Give the extent of all Plasmodium falciparum-infected red blood cells.
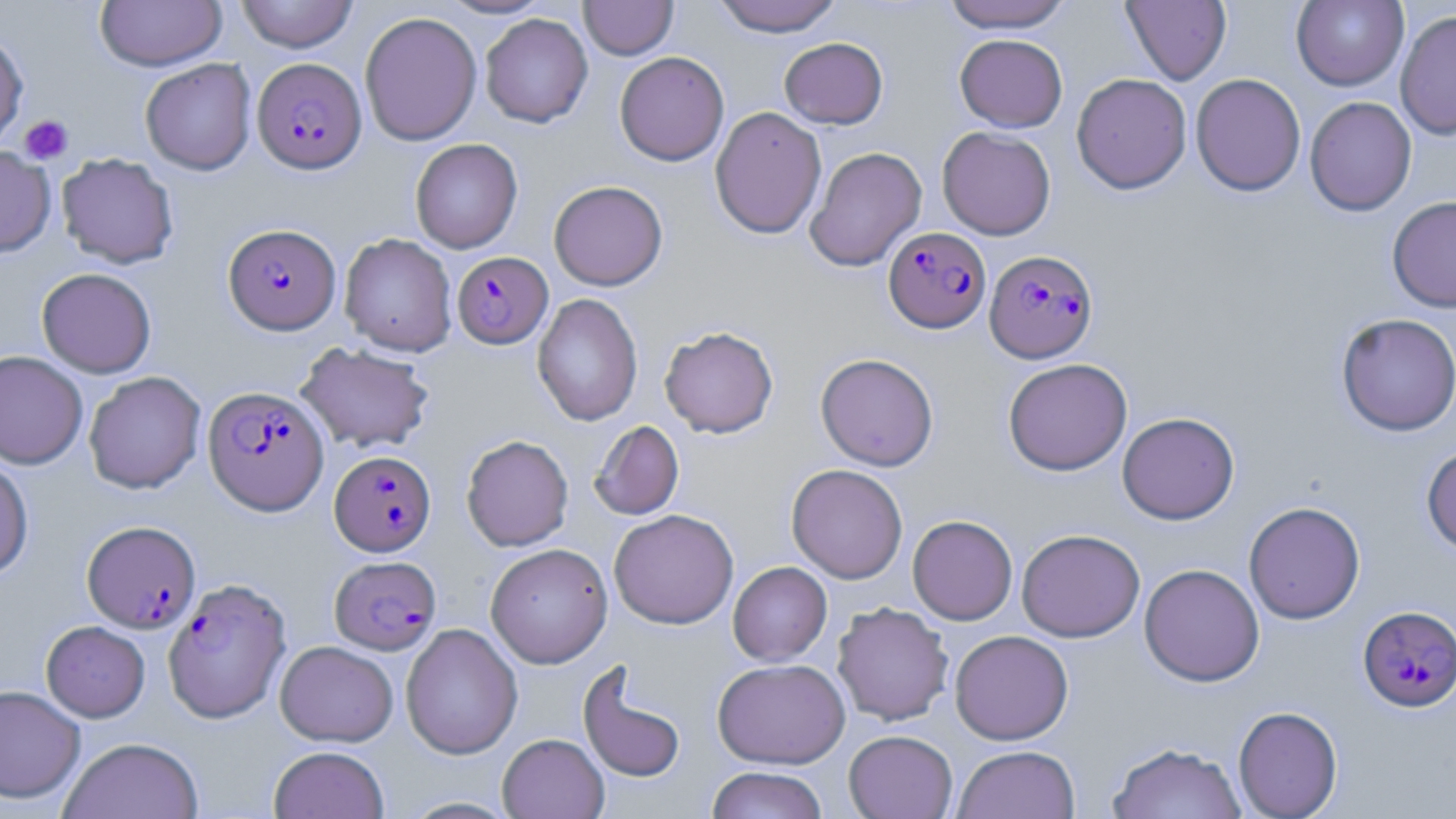

Approximate bounding boxes as (x1,y1)-(x2,y2) corner pairs in pixels.
Plasmodium falciparum-infected red blood cells: (252,57)-(366,173), (223,223)-(340,334), (883,227)-(991,333), (984,249)-(1098,363), (452,251)-(553,348), (203,386)-(329,515), (329,450)-(436,556), (82,520)-(200,633), (329,555)-(441,654), (163,578)-(292,723), (1357,605)-(1456,711).

Summary:
  - Platelet locations: (19,115)-(73,164)
  - Uninfected red blood cell locations: (95,0)-(227,71), (236,0)-(359,52), (438,0)-(554,19), (712,0)-(843,37), (940,0)-(1075,32), (1122,0)-(1231,85), (1291,0)-(1409,91), (579,1)-(678,60), (1395,9)-(1456,141), (359,11)-(482,146), (480,13)-(593,128), (0,30)-(28,150), (955,34)-(1067,132), (779,37)-(888,129), (614,51)-(729,166), (140,58)-(256,175), (1071,73)-(1192,194), (1190,73)-(1306,196), (1304,96)-(1417,216), (710,106)-(827,239), (937,126)-(1056,240), (410,138)-(523,254), (0,146)-(56,257), (805,146)-(927,271), (56,153)-(179,268), (549,180)-(668,290), (1387,195)-(1456,313), (339,233)-(457,356), (36,267)-(156,378), (531,293)-(643,426), (1336,312)-(1456,436), (659,325)-(779,438), (295,342)-(435,454), (0,350)-(88,469), (815,353)-(939,470), (1003,358)-(1132,476), (84,371)-(206,494), (1117,412)-(1239,524), (589,421)-(684,520), (461,434)-(574,551), (1421,445)-(1456,556), (0,455)-(34,582), (786,464)-(908,583), (1243,501)-(1365,624), (609,509)-(738,629), (908,515)-(1018,625), (1017,528)-(1145,642), (485,543)-(613,668), (728,561)-(831,666), (1139,563)-(1265,686), (832,602)-(954,726), (41,620)-(150,722), (401,623)-(523,759), (950,630)-(1073,744), (275,640)-(399,747), (712,658)-(850,768), (578,663)-(686,784), (0,685)-(85,804), (1233,705)-(1343,818), (843,730)-(957,819), (497,733)-(609,819), (59,737)-(203,819), (1108,742)-(1247,819), (268,745)-(390,819), (952,745)-(1080,819), (706,766)-(829,819)
  - Slide-level diagnosis: Plasmodium falciparum
  - Stain: May-Grünwald-Giemsa
  - Magnification: 1000x
  - Image size: 1456×819 pixels
  - Field of view: one of a larger specimen
  - Preparation: thin blood film
  - Modality: light microscopy